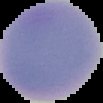
Cell region segmented out of the field of view; the surrounding area is masked to black. From a thin blood film. Result: negative for Plasmodium parasites. Image is 103×103 pixels.